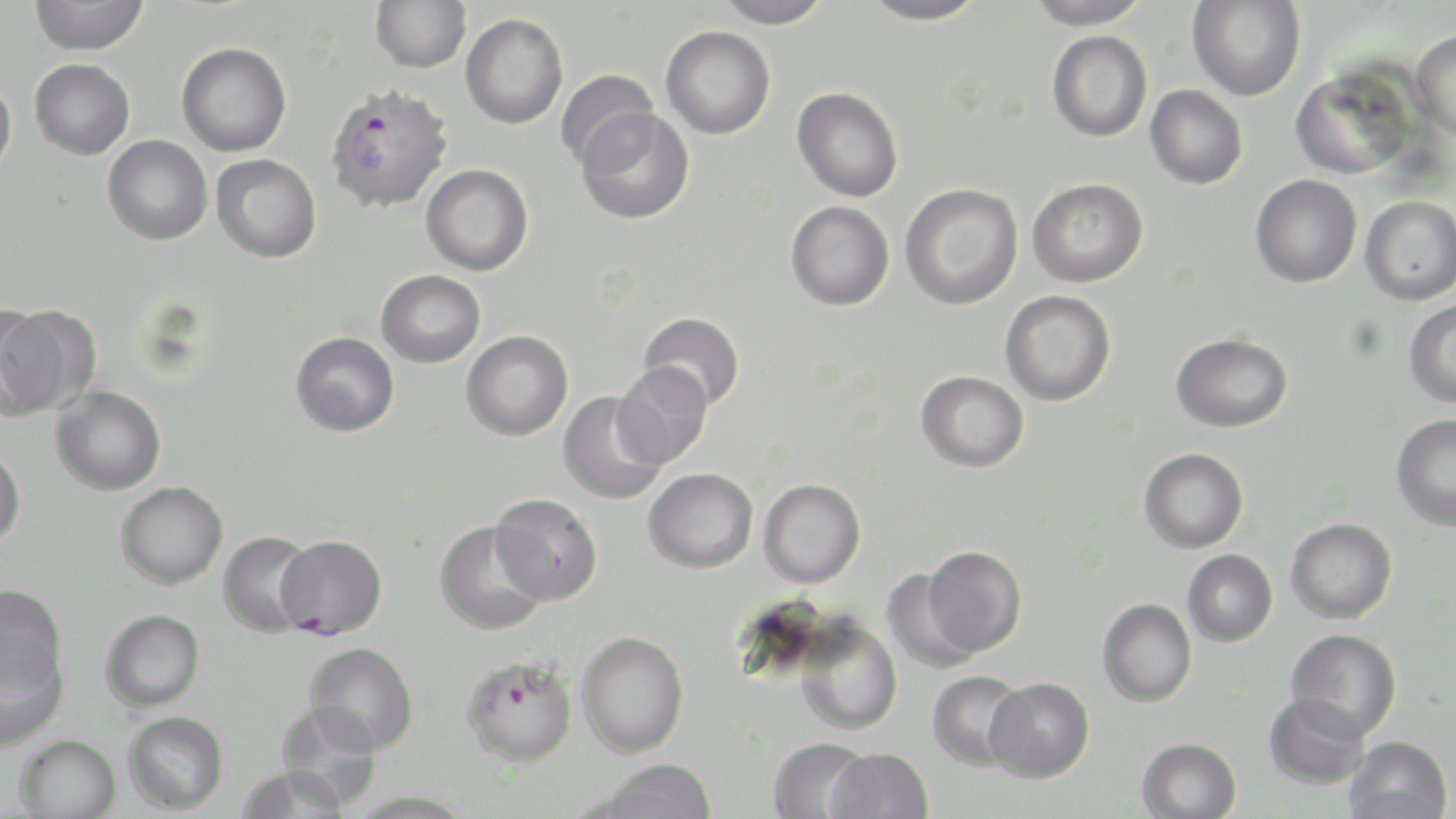
{
  "slide_level_diagnosis": "Plasmodium falciparum",
  "modality": "optical microscopy",
  "field_of_view": "one of a larger specimen",
  "plasmodium_falciparum_infected_red_blood_cell_locations": "approximate bounding boxes as named x1/y1/x2/y2 corners in pixels: (x1=324, y1=82, x2=454, y2=214), (x1=462, y1=654, x2=579, y2=767)",
  "magnification": "1000x",
  "image_size": "1456×819 pixels",
  "uninfected_red_blood_cell_locations": "approximate bounding boxes as named x1/y1/x2/y2 corners in pixels: (x1=29, y1=0, x2=148, y2=55), (x1=371, y1=0, x2=471, y2=72), (x1=711, y1=0, x2=832, y2=28), (x1=859, y1=0, x2=988, y2=25), (x1=1024, y1=0, x2=1153, y2=30), (x1=1187, y1=1, x2=1306, y2=101), (x1=460, y1=13, x2=568, y2=129), (x1=661, y1=25, x2=775, y2=139), (x1=1047, y1=30, x2=1152, y2=142), (x1=1410, y1=30, x2=1456, y2=138), (x1=177, y1=42, x2=292, y2=156), (x1=29, y1=58, x2=135, y2=159), (x1=1290, y1=65, x2=1420, y2=181), (x1=555, y1=70, x2=659, y2=171), (x1=0, y1=72, x2=17, y2=180), (x1=1145, y1=85, x2=1248, y2=189), (x1=792, y1=86, x2=903, y2=202), (x1=576, y1=108, x2=695, y2=224), (x1=103, y1=134, x2=213, y2=244), (x1=211, y1=154, x2=322, y2=263), (x1=421, y1=164, x2=533, y2=276), (x1=1250, y1=174, x2=1362, y2=287), (x1=1027, y1=177, x2=1148, y2=287), (x1=900, y1=183, x2=1023, y2=310), (x1=1360, y1=195, x2=1456, y2=305), (x1=786, y1=200, x2=895, y2=311), (x1=376, y1=269, x2=485, y2=367), (x1=1000, y1=290, x2=1116, y2=406), (x1=1403, y1=298, x2=1456, y2=408), (x1=1, y1=305, x2=101, y2=418), (x1=638, y1=311, x2=745, y2=411), (x1=461, y1=330, x2=573, y2=441), (x1=291, y1=331, x2=400, y2=436), (x1=1171, y1=332, x2=1292, y2=432), (x1=612, y1=361, x2=712, y2=469), (x1=916, y1=370, x2=1029, y2=472), (x1=50, y1=385, x2=166, y2=495), (x1=557, y1=391, x2=667, y2=505), (x1=1391, y1=414, x2=1456, y2=531), (x1=0, y1=445, x2=25, y2=549), (x1=1139, y1=448, x2=1248, y2=553), (x1=643, y1=467, x2=758, y2=573), (x1=758, y1=478, x2=866, y2=588), (x1=115, y1=481, x2=228, y2=589), (x1=489, y1=493, x2=603, y2=605), (x1=1286, y1=517, x2=1397, y2=624), (x1=435, y1=521, x2=548, y2=635), (x1=218, y1=530, x2=318, y2=638), (x1=276, y1=535, x2=386, y2=638), (x1=923, y1=546, x2=1027, y2=656), (x1=1182, y1=549, x2=1278, y2=647), (x1=881, y1=570, x2=985, y2=675), (x1=0, y1=583, x2=68, y2=700), (x1=1097, y1=598, x2=1197, y2=707), (x1=99, y1=609, x2=206, y2=712), (x1=793, y1=616, x2=903, y2=735), (x1=1285, y1=629, x2=1402, y2=738), (x1=576, y1=630, x2=689, y2=757), (x1=0, y1=641, x2=68, y2=751), (x1=304, y1=642, x2=418, y2=754), (x1=927, y1=670, x2=1028, y2=770), (x1=985, y1=677, x2=1095, y2=782), (x1=1263, y1=693, x2=1371, y2=789), (x1=275, y1=700, x2=383, y2=810), (x1=123, y1=711, x2=229, y2=814), (x1=15, y1=734, x2=122, y2=819), (x1=1343, y1=735, x2=1452, y2=819), (x1=767, y1=737, x2=874, y2=818), (x1=1136, y1=737, x2=1242, y2=819), (x1=826, y1=748, x2=934, y2=819), (x1=594, y1=758, x2=718, y2=818), (x1=235, y1=764, x2=351, y2=818), (x1=347, y1=789, x2=475, y2=818)",
  "stain": "May-Grünwald-Giemsa",
  "preparation": "thin blood film"
}